Classify this cell by malaria status.
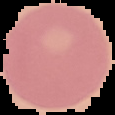
It is uninfected.

Image is 115×115 pixels. The area outside the segmented cell region is set to black. From a thin blood smear.